Classify this cell by malaria status.
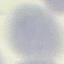
Uninfected.

Summary:
  - Image type: cell patch, automatically extracted from a larger field of view and resized to 64 × 64 pixels
  - Stain: Giemsa
  - Preparation: thin smear
  - Capture: smartphone camera at the microscope eyepiece